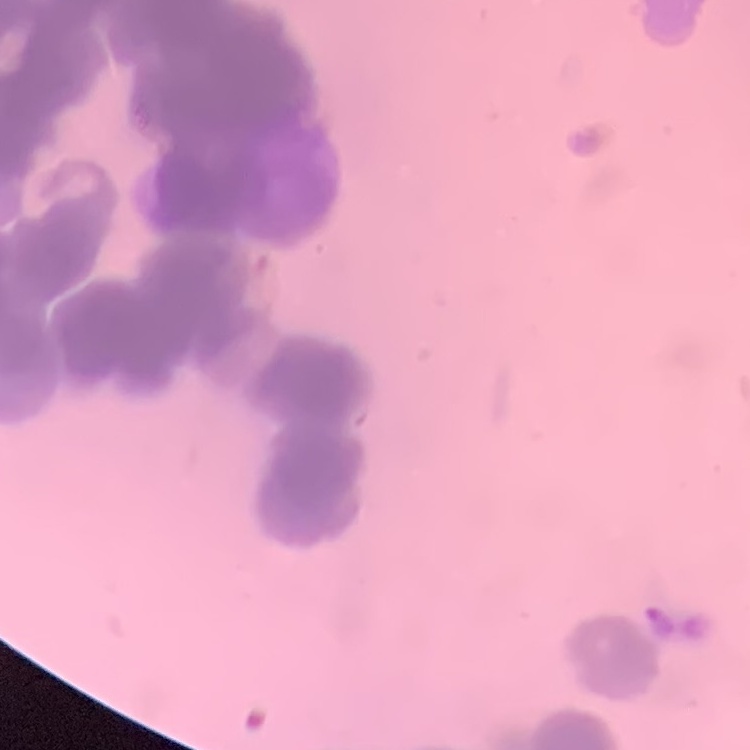

erythrocyte morphology = rouleaux formation
stain = Field's or Giemsa
image type = square crop of a larger photomicrograph
preparation = thin blood film